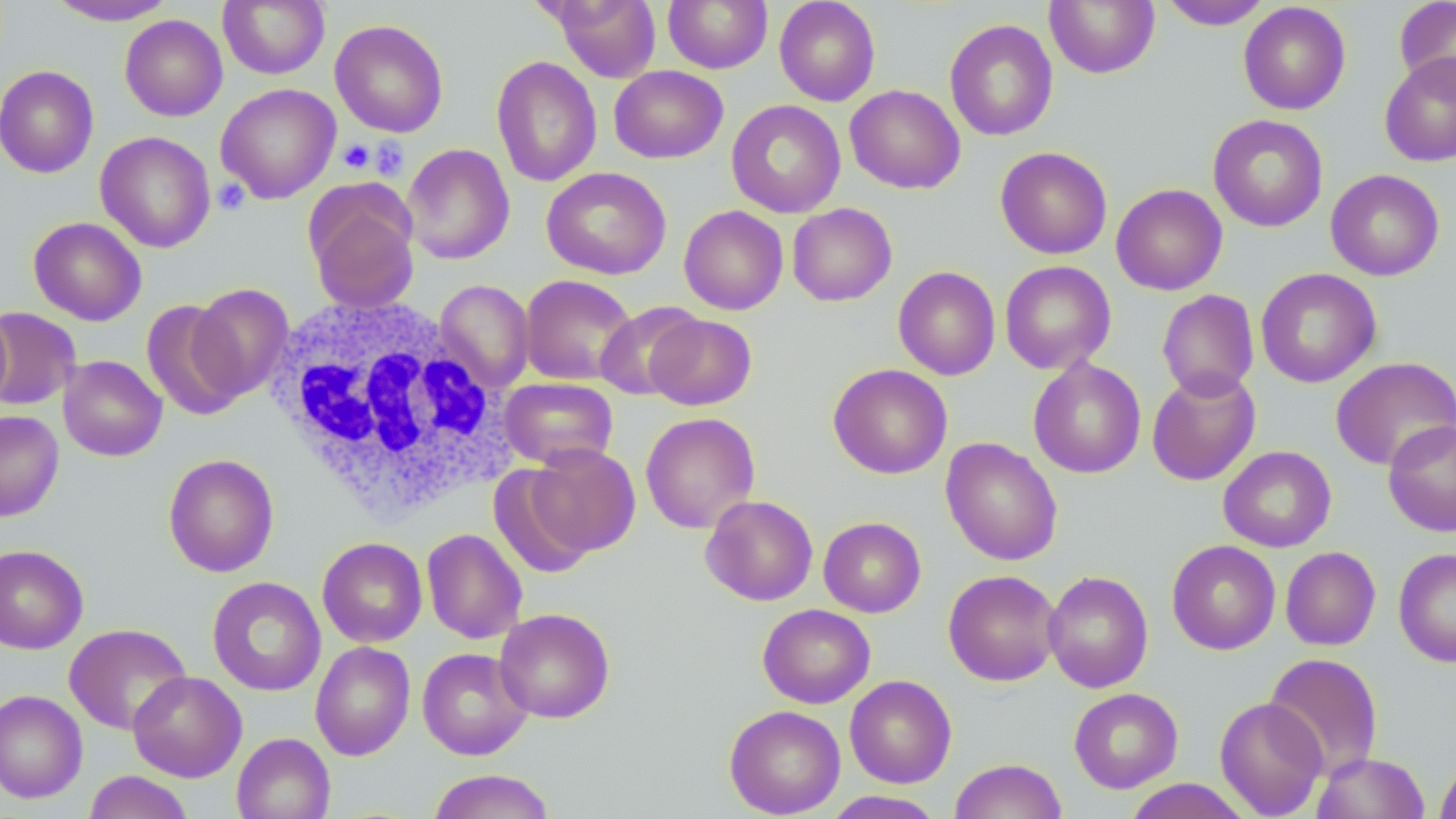
slide-level diagnosis = negative for blood parasites
uninfected red blood cell locations = approximate bounding boxes as (x1, y1, x2, y2) in pixels: (46, 0, 179, 25), (218, 0, 330, 79), (553, 0, 660, 82), (663, 0, 772, 74), (774, 0, 880, 106), (1393, 0, 1456, 96), (1044, 1, 1160, 78), (1158, 1, 1275, 30), (1238, 2, 1351, 115), (120, 15, 227, 121), (330, 19, 449, 137), (944, 19, 1059, 142), (1379, 52, 1456, 167), (491, 55, 602, 187), (0, 65, 100, 178), (609, 65, 728, 163), (215, 84, 341, 203), (844, 85, 965, 194), (726, 99, 846, 217), (1208, 114, 1328, 232), (95, 131, 215, 253), (401, 143, 515, 265), (995, 146, 1112, 259), (542, 167, 671, 280), (1325, 169, 1445, 280), (1111, 183, 1228, 295), (305, 184, 421, 313), (787, 203, 897, 306), (679, 205, 789, 315), (28, 216, 147, 325), (999, 260, 1116, 374), (893, 266, 1001, 380), (1255, 268, 1382, 388), (520, 274, 636, 385), (435, 279, 534, 392), (188, 283, 294, 401), (1157, 290, 1260, 400), (142, 299, 248, 420), (595, 301, 704, 400), (0, 307, 81, 411), (0, 309, 14, 410), (645, 314, 757, 410), (59, 355, 167, 461), (1027, 357, 1146, 479), (1330, 357, 1456, 471), (828, 363, 953, 479), (1147, 368, 1261, 486), (500, 378, 618, 470), (0, 410, 64, 522), (640, 412, 761, 534), (1383, 419, 1456, 536), (941, 437, 1063, 566), (528, 444, 640, 556), (1218, 445, 1336, 552), (163, 453, 280, 577), (488, 466, 596, 579), (700, 495, 818, 606), (818, 516, 926, 617), (421, 528, 527, 644), (317, 537, 427, 647), (1166, 540, 1281, 655), (0, 544, 89, 654), (1280, 546, 1381, 650), (1393, 547, 1456, 668), (943, 569, 1062, 686), (1043, 570, 1154, 693), (207, 576, 326, 696), (757, 604, 875, 708), (494, 607, 615, 723), (63, 623, 191, 735), (310, 641, 416, 761), (417, 647, 533, 760), (1264, 652, 1384, 778), (128, 671, 247, 782), (844, 675, 957, 788), (1069, 688, 1183, 793), (0, 689, 88, 803), (1214, 696, 1328, 817), (724, 704, 846, 818), (232, 732, 335, 819), (1312, 752, 1430, 818), (949, 758, 1067, 819), (1434, 760, 1456, 818), (427, 769, 557, 819), (83, 770, 194, 819), (1122, 779, 1253, 818), (821, 790, 946, 819)
magnification = 1000x
modality = light microscopy
image size = 1456×819 pixels
platelet locations = approximate bounding boxes as (x1, y1, x2, y2) in pixels: (368, 136, 409, 180), (338, 138, 375, 174), (213, 178, 250, 215)
stain = May-Grünwald-Giemsa
white blood cell locations = approximate bounding boxes as (x1, y1, x2, y2) in pixels: (266, 292, 511, 518)
preparation = thin blood smear
field of view = one of a larger specimen